Name the blood parasite species.
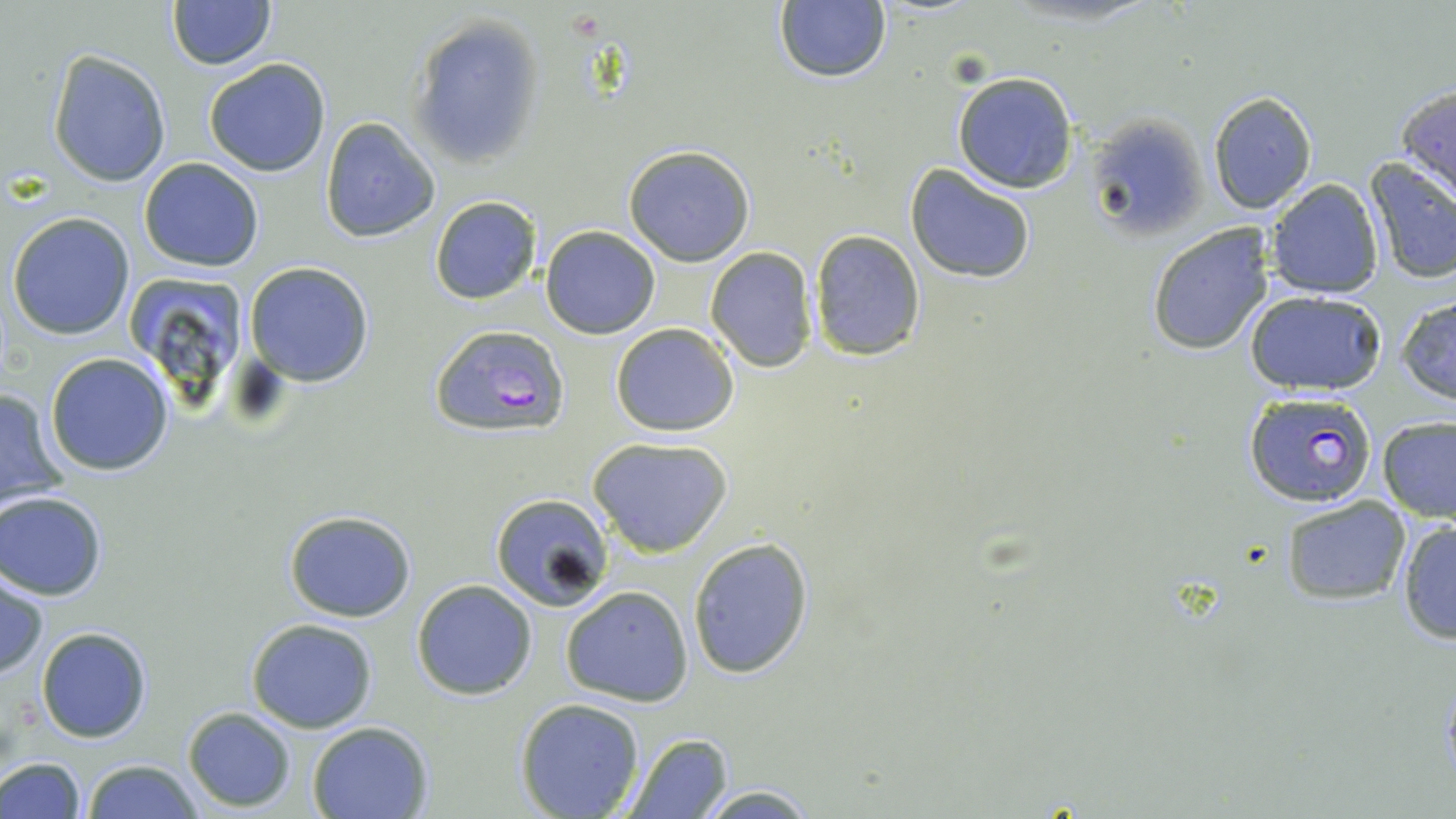

Plasmodium falciparum.

Approximate bounding boxes as (x1,y1)-(x2,y2) corner pairs in pixels. Plasmodium falciparum-infected red blood cell locations: (430,324)-(572,440), (1248,395)-(1380,509). Uninfected red blood cell locations: (168,0)-(275,70), (774,1)-(890,85), (407,14)-(545,169), (48,49)-(172,188), (203,58)-(332,176), (951,72)-(1077,193), (1395,83)-(1456,203), (1208,90)-(1318,212), (319,117)-(440,242), (1090,117)-(1207,241), (622,143)-(755,266), (139,157)-(264,273), (1362,159)-(1456,284), (904,166)-(1036,283), (1264,179)-(1383,299), (429,196)-(540,305), (7,212)-(134,339), (1146,224)-(1276,356), (541,225)-(661,340), (806,230)-(925,361), (704,246)-(818,371), (244,261)-(374,387), (127,279)-(247,385), (1246,291)-(1388,395), (1396,293)-(1456,405), (610,322)-(740,436), (45,351)-(176,476), (0,384)-(72,513), (1377,416)-(1456,521), (587,435)-(734,558), (1,491)-(108,600), (488,492)-(615,610), (1280,495)-(1410,604), (283,509)-(417,623), (1396,520)-(1456,644), (687,537)-(815,677), (1,572)-(48,680), (410,579)-(537,700), (559,585)-(694,705), (246,619)-(378,733), (36,626)-(153,744), (514,698)-(645,819), (182,707)-(296,810), (307,720)-(435,818), (619,731)-(733,817), (0,757)-(85,819), (81,759)-(204,819), (692,783)-(821,817). Thin blood smear. May-Grünwald-Giemsa-stained preparation. 1000x magnification. Image is 1456×819 pixels. Light microscopy. Single field of view.